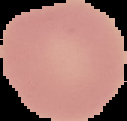

From a thin blood film. Cell region segmented out of the field of view; the surrounding area is masked to black. Result: no malaria parasites seen. Image is 127×121 pixels.